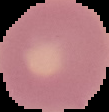
malaria status = uninfected
image size = 109×112 pixels
preparation = thin blood film
image type = segmented cell region on a black background